Assess this cell for malaria.
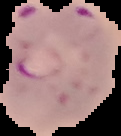

Parasitized.

From a thin blood smear. Image is 121×136 pixels. Cell region segmented out of the field of view; the surrounding area is masked to black.